Locate every uninfected red blood cell.
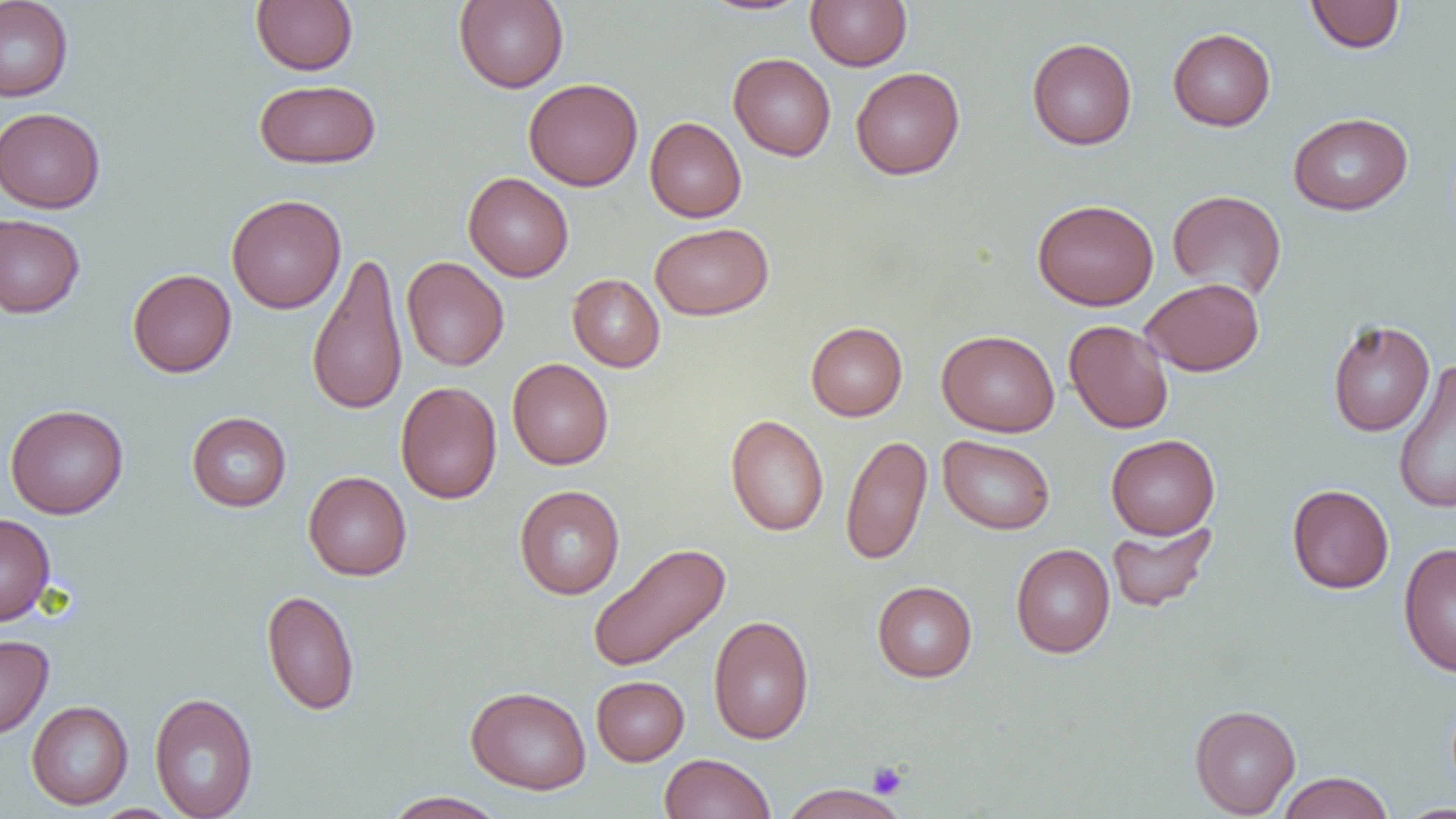

Approximate bounding boxes as (x1,y1)-(x2,y2) corner pairs in pixels.
Uninfected red blood cells: (0,0)-(73,102), (251,0)-(358,75), (698,0)-(813,16), (806,0)-(912,71), (454,1)-(569,92), (1305,1)-(1405,53), (1168,28)-(1276,131), (1027,38)-(1137,150), (728,53)-(836,161), (851,67)-(965,180), (523,78)-(643,191), (254,79)-(381,169), (0,107)-(106,213), (1288,112)-(1413,215), (645,117)-(747,222), (463,172)-(574,282), (1167,190)-(1287,301), (226,194)-(346,314), (1032,199)-(1159,311), (0,214)-(85,318), (650,222)-(773,320), (306,251)-(408,417), (401,256)-(509,371), (127,269)-(236,377), (567,274)-(665,372), (1141,278)-(1264,376), (1064,319)-(1174,434), (1327,319)-(1435,437), (806,322)-(907,421), (937,330)-(1060,437), (507,358)-(613,470), (1393,360)-(1456,515), (395,381)-(502,504), (5,404)-(129,519), (187,412)-(291,512), (725,414)-(828,536), (841,434)-(933,566), (1106,434)-(1220,539), (938,435)-(1056,534), (303,471)-(412,581), (1287,484)-(1394,593), (514,485)-(625,599), (0,513)-(55,626), (1106,520)-(1218,613), (1398,542)-(1456,677), (587,543)-(730,672), (1011,543)-(1115,658), (872,580)-(977,682), (261,589)-(360,715), (708,615)-(814,744), (0,634)-(54,739), (591,675)-(689,766), (465,686)-(591,794), (149,692)-(258,819), (27,701)-(133,810), (1190,704)-(1301,817), (659,752)-(776,819), (1277,772)-(1394,819), (779,783)-(909,819), (381,791)-(508,819), (1396,803)-(1456,818), (90,804)-(185,819).

Summary:
  - Platelet locations: (867,761)-(909,798)
  - Slide-level diagnosis: no evidence of blood parasites
  - Preparation: thin blood film
  - Magnification: 1000x
  - Image size: 1456×819 pixels
  - Field of view: one of a larger specimen
  - Modality: optical microscopy